Outline each blood parasite and name the species.
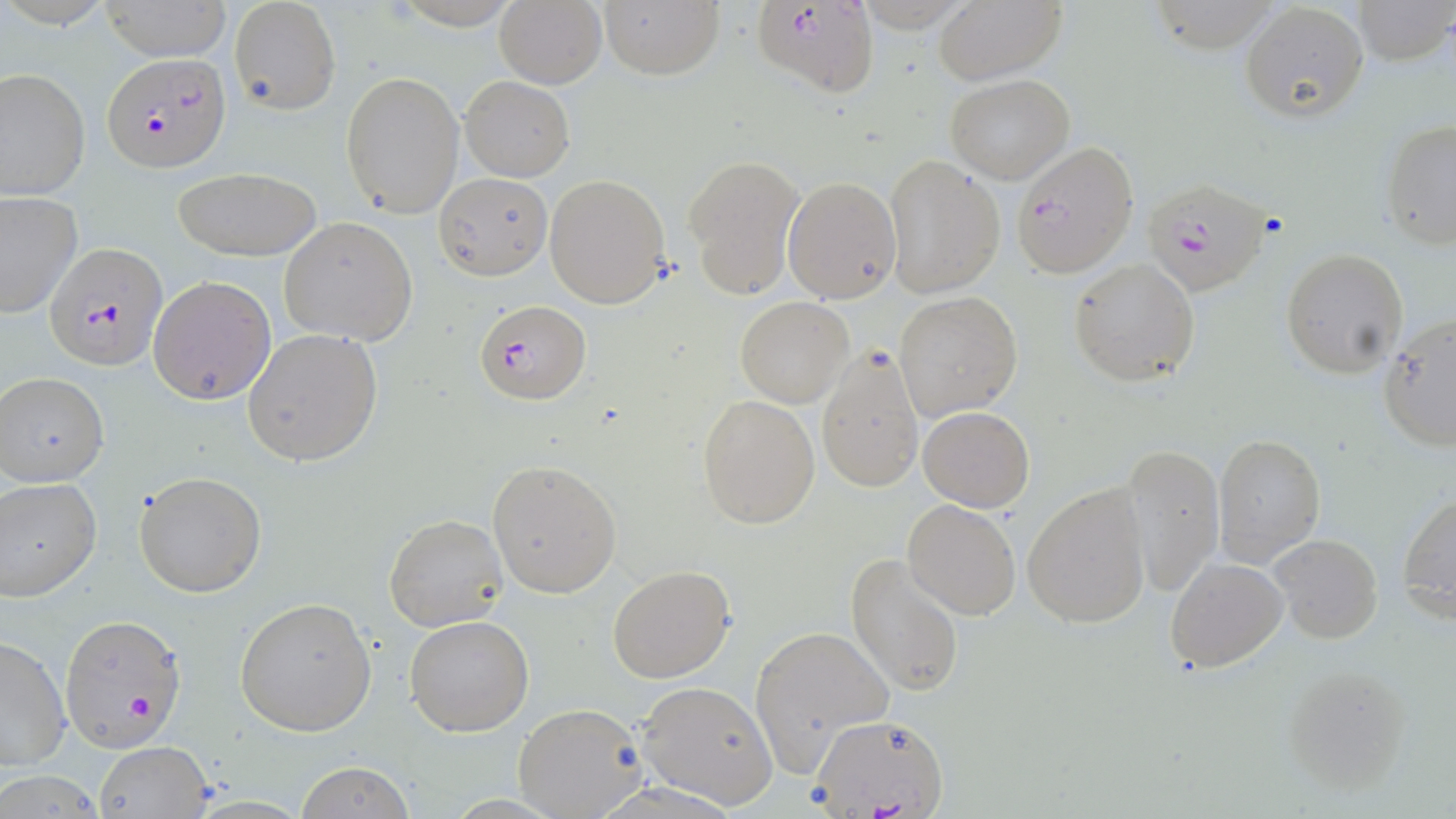
Approximate bounding boxes as (x1,y1)-(x2,y2) corner pairs in pixels.
Plasmodium falciparum-infected red blood cells: (752,2)-(880,99), (102,50)-(230,170), (1010,140)-(1138,277), (1142,179)-(1273,297), (45,243)-(167,371), (478,298)-(588,406), (60,615)-(186,751), (812,713)-(949,817).
No Plasmodium ovale, Plasmodium malariae, Plasmodium vivax, Babesia divergens, or Trypanosoma brucei observed.

Summary:
  - Uninfected red blood cell locations: (99,0)-(232,61), (228,0)-(340,116), (494,0)-(607,89), (598,0)-(724,80), (933,0)-(1066,85), (1353,0)-(1454,66), (1238,3)-(1368,123), (1,67)-(91,199), (340,70)-(464,219), (945,73)-(1074,184), (459,75)-(575,182), (1380,119)-(1456,249), (883,155)-(1005,299), (685,156)-(803,299), (169,167)-(324,260), (435,173)-(553,279), (545,174)-(670,308), (782,176)-(902,303), (0,191)-(81,319), (279,217)-(417,346), (1281,248)-(1408,378), (1068,257)-(1199,386), (148,274)-(277,406), (894,292)-(1022,422), (736,297)-(852,407), (1377,314)-(1456,452), (243,327)-(385,468), (815,348)-(925,494), (0,372)-(109,488), (697,394)-(820,528), (917,405)-(1035,511), (1212,433)-(1325,567), (1122,442)-(1223,597), (487,460)-(622,598), (134,471)-(267,597), (0,477)-(102,603), (1022,484)-(1149,630), (1398,491)-(1456,618), (901,499)-(1022,620), (383,513)-(509,633), (1268,535)-(1383,642), (845,552)-(966,699), (1165,557)-(1288,671), (606,566)-(734,683), (234,598)-(376,736), (404,616)-(533,737), (749,623)-(895,776), (0,637)-(71,772), (1280,663)-(1414,795), (635,680)-(778,809), (514,701)-(648,817), (95,739)-(213,818), (292,763)-(417,819)
  - Slide-level diagnosis: Plasmodium falciparum
  - Modality: light microscopy
  - Field of view: one of a larger specimen
  - Preparation: thin blood smear
  - Image size: 1456×819 pixels
  - Stain: May-Grünwald-Giemsa
  - Magnification: 1000x